Outline each blood parasite and name the species.
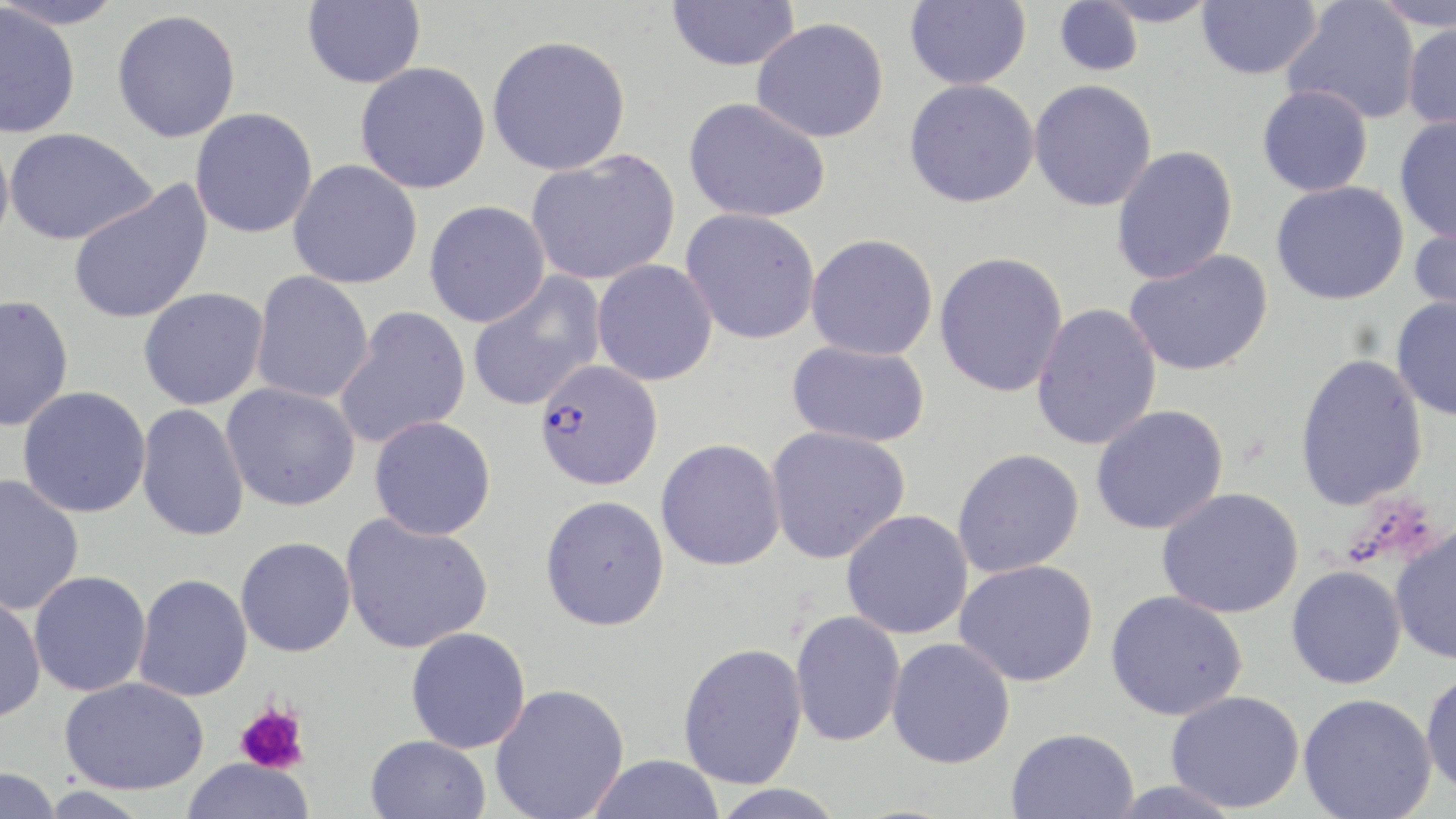
Approximate bounding boxes as (x1, y1, x2, y2) in pixels.
Plasmodium falciparum-infected red blood cells: (533, 359, 663, 491).
No Plasmodium ovale, Plasmodium malariae, Plasmodium vivax, Babesia divergens, or Trypanosoma brucei observed.

slide-level diagnosis = Plasmodium falciparum
magnification = 1000x
platelet locations = approximate bounding boxes as (x1, y1, x2, y2) in pixels: (234, 701, 311, 774)
modality = light microscopy
field of view = single
image size = 1456×819 pixels
uninfected red blood cell locations = approximate bounding boxes as (x1, y1, x2, y2) in pixels: (0, 0, 127, 29), (302, 0, 426, 89), (666, 0, 801, 72), (905, 0, 1031, 90), (1095, 0, 1220, 27), (1196, 0, 1323, 80), (1370, 0, 1456, 31), (1053, 1, 1144, 77), (1282, 1, 1421, 124), (0, 5, 81, 139), (112, 9, 241, 142), (751, 17, 889, 143), (1401, 20, 1456, 132), (486, 35, 632, 175), (355, 61, 492, 193), (904, 79, 1040, 208), (1029, 79, 1158, 212), (1257, 85, 1373, 197), (683, 97, 831, 223), (190, 107, 319, 238), (1394, 114, 1456, 243), (0, 127, 15, 256), (4, 127, 156, 245), (1111, 145, 1238, 284), (526, 149, 682, 286), (288, 159, 423, 289), (68, 179, 214, 326), (1271, 180, 1410, 305), (424, 200, 550, 327), (681, 208, 822, 344), (1409, 220, 1456, 329), (806, 233, 938, 360), (1124, 249, 1273, 377), (934, 251, 1069, 398), (591, 259, 719, 386), (250, 271, 374, 405), (467, 272, 606, 412), (137, 287, 270, 410), (0, 295, 74, 432), (1390, 296, 1456, 422), (1030, 303, 1162, 451), (334, 305, 471, 449), (786, 340, 931, 448), (1294, 352, 1428, 511), (222, 382, 361, 511), (17, 386, 152, 519), (136, 403, 250, 542), (1090, 405, 1229, 535), (368, 415, 497, 540), (765, 426, 911, 564), (656, 438, 786, 571), (952, 448, 1085, 578), (0, 474, 84, 616), (1156, 487, 1304, 619), (540, 495, 670, 631), (841, 510, 973, 639), (340, 515, 494, 654), (1390, 524, 1456, 665), (235, 536, 356, 658), (954, 559, 1098, 687), (1286, 565, 1407, 690), (28, 570, 152, 697), (133, 574, 253, 702), (1105, 590, 1247, 720), (0, 592, 46, 723), (789, 610, 906, 746), (405, 627, 531, 753), (887, 638, 1016, 769), (677, 641, 808, 789), (1420, 666, 1456, 801), (58, 677, 209, 795), (490, 683, 630, 819), (1166, 690, 1305, 813), (1298, 693, 1437, 819), (1006, 727, 1139, 818), (365, 735, 491, 819), (586, 754, 727, 819), (179, 758, 317, 819), (0, 767, 62, 819), (708, 784, 849, 818)
stain = May-Grünwald-Giemsa
preparation = thin blood smear